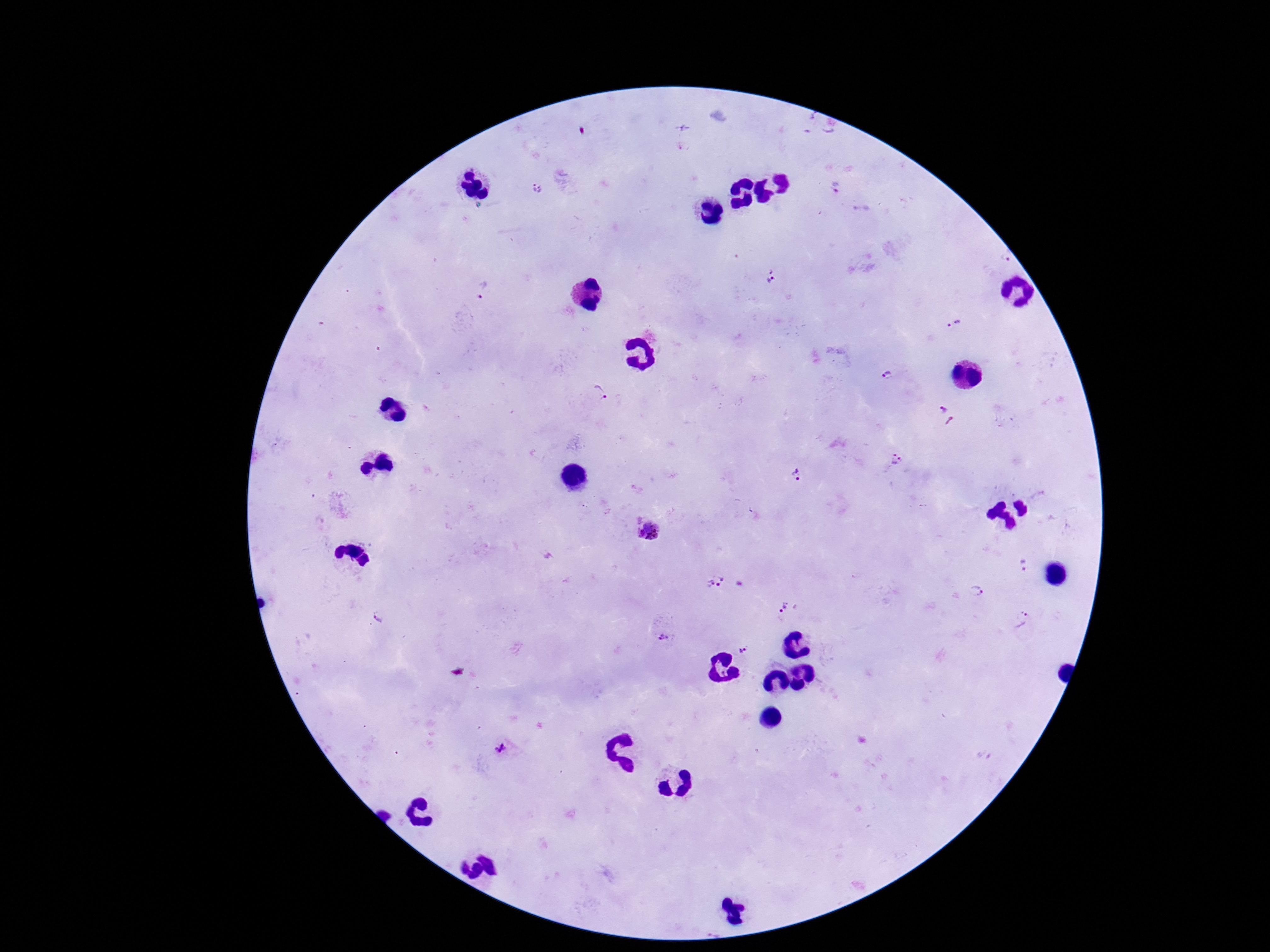

stain = Giemsa
image size = 1270×952 pixels
patient malaria status = positive
magnification = 100x
preparation = thick peripheral-blood smear
Plasmodium parasite locations = approximate centers as {x, y} in pixels: {836, 186}, {536, 190}, {773, 275}, {483, 290}, {955, 324}, {886, 373}, {600, 392}, {947, 416}, {896, 458}, {795, 475}, {647, 531}, {1025, 568}, {713, 579}, {975, 590}, {783, 605}, {378, 616}, {1021, 620}, {663, 637}, {743, 649}, {502, 749}
capture = smartphone camera through the microscope eyepiece
field of view = single